State the blood parasite species.
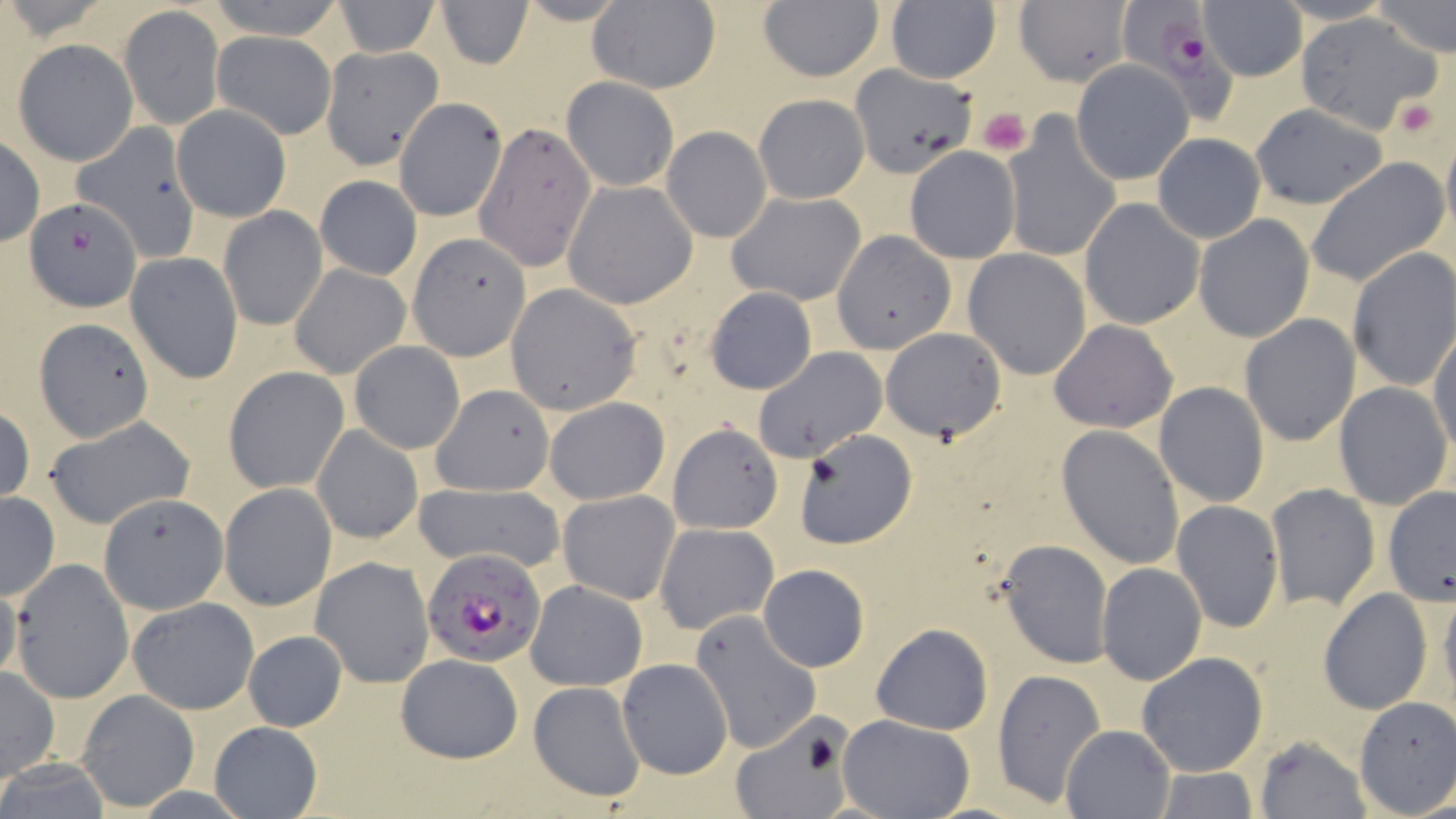
Plasmodium falciparum.

image size = 1456×819 pixels
modality = light microscopy
preparation = thin blood film
uninfected red blood cell locations = approximate bounding boxes as [x1, y1, x2, y2] in pixels: [204, 0, 345, 38], [331, 0, 440, 57], [435, 0, 534, 69], [883, 0, 1002, 85], [1372, 0, 1456, 57], [1013, 1, 1132, 87], [586, 2, 721, 94], [757, 2, 884, 82], [1198, 2, 1306, 81], [118, 6, 224, 130], [1295, 14, 1440, 130], [39, 21, 219, 145], [212, 31, 336, 137], [14, 39, 137, 165], [305, 41, 440, 168], [1071, 60, 1193, 185], [850, 66, 975, 178], [561, 76, 679, 193], [755, 93, 869, 204], [393, 95, 507, 222], [171, 103, 291, 222], [1249, 104, 1389, 209], [1002, 117, 1121, 262], [474, 121, 599, 273], [73, 124, 201, 260], [661, 127, 772, 244], [1440, 131, 1456, 248], [1153, 132, 1265, 243], [0, 133, 45, 248], [904, 146, 1021, 264], [1309, 158, 1448, 286], [314, 174, 422, 279], [563, 180, 697, 309], [726, 192, 866, 308], [24, 195, 142, 312], [1079, 199, 1204, 330], [219, 204, 326, 331], [1193, 215, 1314, 343], [833, 232, 956, 354], [408, 233, 531, 360], [1347, 248, 1456, 392], [963, 250, 1092, 378], [127, 251, 244, 383], [290, 264, 410, 380], [505, 284, 642, 416], [704, 285, 818, 395], [1239, 313, 1362, 446], [35, 319, 153, 441], [1049, 320, 1178, 433], [880, 327, 1007, 442], [1428, 329, 1456, 456], [349, 341, 465, 455], [752, 346, 887, 463], [224, 367, 349, 494], [1333, 381, 1454, 508], [1153, 382, 1270, 506], [430, 383, 556, 496], [543, 396, 669, 504], [0, 406, 35, 506], [42, 417, 196, 530], [667, 423, 782, 534], [313, 424, 423, 544], [1056, 425, 1184, 568], [794, 430, 916, 548], [411, 482, 565, 572], [218, 483, 336, 610], [1267, 484, 1379, 609], [1382, 486, 1456, 607], [558, 489, 680, 605], [0, 491, 59, 601], [99, 493, 229, 622], [1172, 500, 1284, 631], [655, 523, 779, 635], [998, 539, 1113, 668], [310, 556, 434, 687], [11, 562, 134, 702], [759, 563, 869, 671], [1096, 563, 1207, 685], [525, 579, 648, 691], [0, 582, 24, 691], [1439, 589, 1456, 710], [1319, 590, 1432, 715], [128, 597, 257, 713], [690, 610, 821, 756], [870, 622, 993, 735], [244, 630, 348, 733], [1135, 650, 1268, 776], [395, 653, 523, 762], [617, 657, 733, 780], [0, 666, 58, 783], [991, 668, 1106, 808], [526, 680, 647, 804], [75, 689, 200, 812], [1352, 696, 1456, 817], [837, 714, 974, 819], [729, 715, 856, 819], [211, 720, 321, 817], [1061, 724, 1175, 818], [1253, 734, 1371, 819], [1152, 766, 1260, 819]
magnification = 1000x
Plasmodium falciparum-infected red blood cell locations = approximate bounding boxes as [x1, y1, x2, y2] in pixels: [1122, 2, 1235, 122], [423, 549, 550, 668]
platelet locations = approximate bounding boxes as [x1, y1, x2, y2] in pixels: [1390, 97, 1443, 139], [976, 106, 1033, 157]
stain = May-Grünwald-Giemsa
field of view = one of a larger specimen